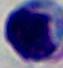
A white blood cell is seen. Micrograph. Captured at 1000x magnification.